Locate and identify every blood parasite.
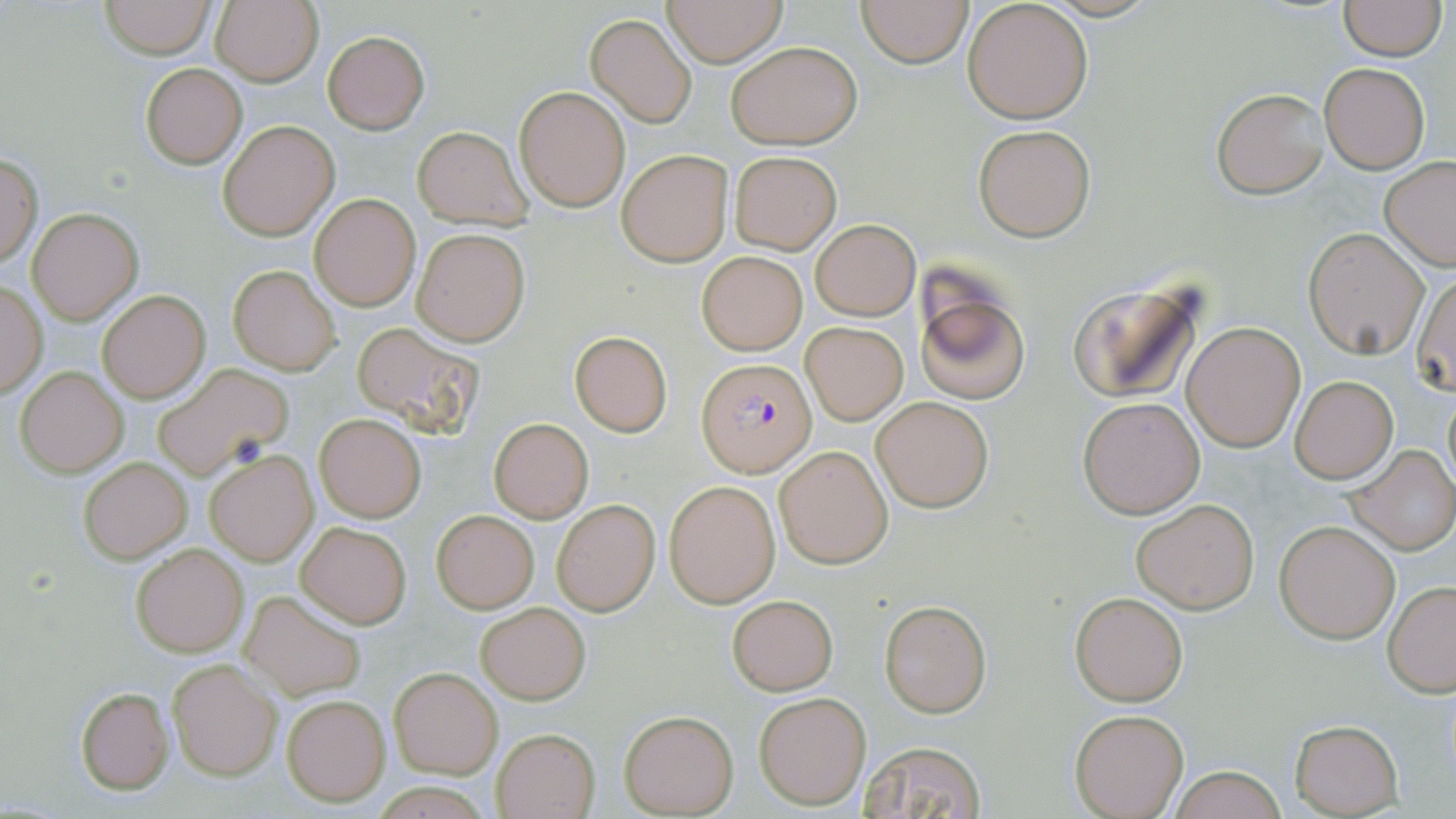
Approximate bounding boxes as [x1, y1, x2, y2] in pixels.
Plasmodium falciparum-infected red blood cells: [698, 359, 813, 475].
No Plasmodium ovale, Plasmodium malariae, Plasmodium vivax, Babesia divergens, or Trypanosoma brucei observed.

Summary:
  - Uninfected red blood cell locations: [210, 0, 323, 87], [660, 0, 788, 66], [856, 0, 975, 68], [97, 1, 217, 57], [962, 1, 1093, 122], [1337, 1, 1448, 61], [585, 13, 698, 127], [323, 31, 429, 133], [724, 39, 863, 150], [1320, 63, 1428, 172], [140, 64, 247, 168], [515, 85, 630, 211], [1211, 87, 1329, 199], [220, 121, 338, 240], [971, 124, 1095, 242], [413, 126, 531, 230], [617, 148, 733, 266], [729, 150, 841, 253], [1, 155, 42, 268], [1380, 157, 1456, 271], [310, 193, 421, 311], [27, 208, 142, 323], [810, 219, 920, 320], [1304, 227, 1430, 360], [412, 228, 529, 346], [697, 252, 807, 354], [228, 264, 342, 376], [1411, 272, 1455, 397], [1067, 275, 1212, 406], [913, 280, 1030, 405], [0, 282, 48, 398], [96, 288, 211, 404], [800, 321, 908, 425], [1182, 321, 1306, 452], [351, 322, 483, 439], [569, 330, 673, 438], [151, 361, 292, 478], [15, 365, 128, 477], [1290, 376, 1397, 484], [1441, 384, 1455, 495], [871, 395, 995, 512], [1078, 395, 1204, 518], [315, 413, 425, 522], [489, 418, 593, 522], [1345, 444, 1456, 557], [775, 445, 893, 568], [207, 452, 317, 565], [79, 457, 191, 564], [666, 481, 780, 608], [552, 499, 660, 615], [1131, 499, 1260, 613], [431, 510, 539, 612], [1275, 518, 1401, 643], [296, 522, 410, 629], [130, 541, 249, 657], [1383, 580, 1456, 696], [242, 591, 367, 702], [1071, 592, 1186, 706], [727, 594, 837, 694], [879, 600, 990, 716], [476, 602, 590, 704], [168, 659, 280, 781], [390, 668, 501, 779], [75, 686, 174, 794], [753, 690, 871, 811], [280, 692, 391, 806], [1070, 709, 1188, 819], [619, 710, 738, 816], [1288, 719, 1404, 816], [493, 727, 600, 818], [858, 740, 986, 818], [1164, 767, 1288, 819]
  - Slide-level diagnosis: Plasmodium falciparum
  - Modality: optical microscopy
  - Stain: May-Grünwald-Giemsa
  - Field of view: one of a larger specimen
  - Preparation: thin blood film
  - Image size: 1456×819 pixels
  - Magnification: 1000x